Assess this cell for malaria.
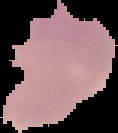
Parasitized.

Summary:
  - Preparation: thin blood smear
  - Image size: 118×133 pixels
  - Image type: cell region segmented out of the field of view; surrounding area masked to black